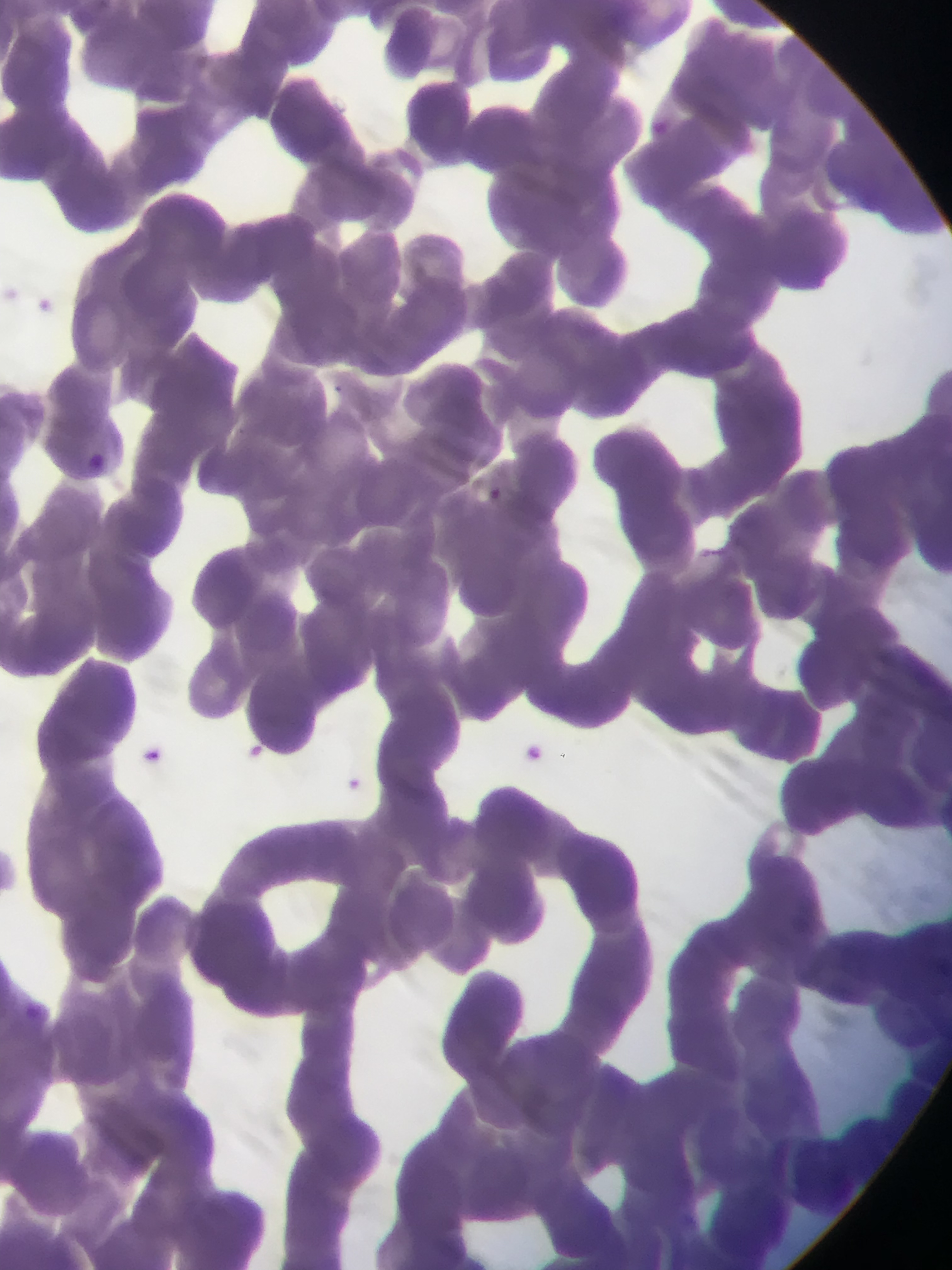

preparation: thin blood smear
capture: mobile-phone photograph through a microscope
plasmodium_parasite_locations: 'approximate bounding boxes as {left, top, right, bottom} in pixels: {84, 453, 120, 493}, {490, 486, 503, 500}, {514, 729, 549, 760}, {236, 736, 276, 767}, {136, 742, 169, 760}, {340, 771, 366, 809}, {20, 994, 51, 1020}'
field_of_view: single
country: Ghana
image_size: 952×1270 pixels